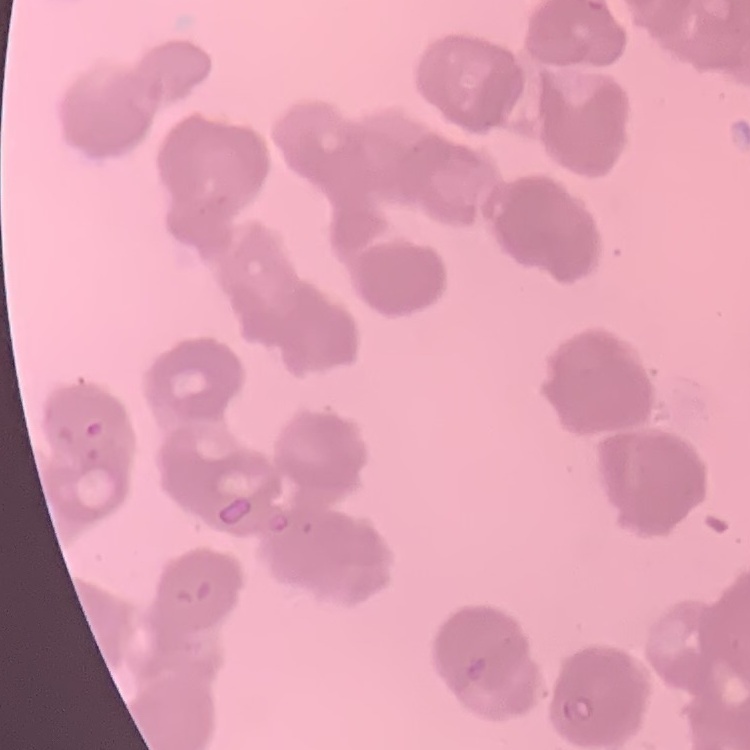
Summary:
  - Erythrocyte morphology: rouleaux formation
  - Preparation: thin blood smear
  - Image type: square crop of a larger photomicrograph
  - Stain: Field's or Giemsa